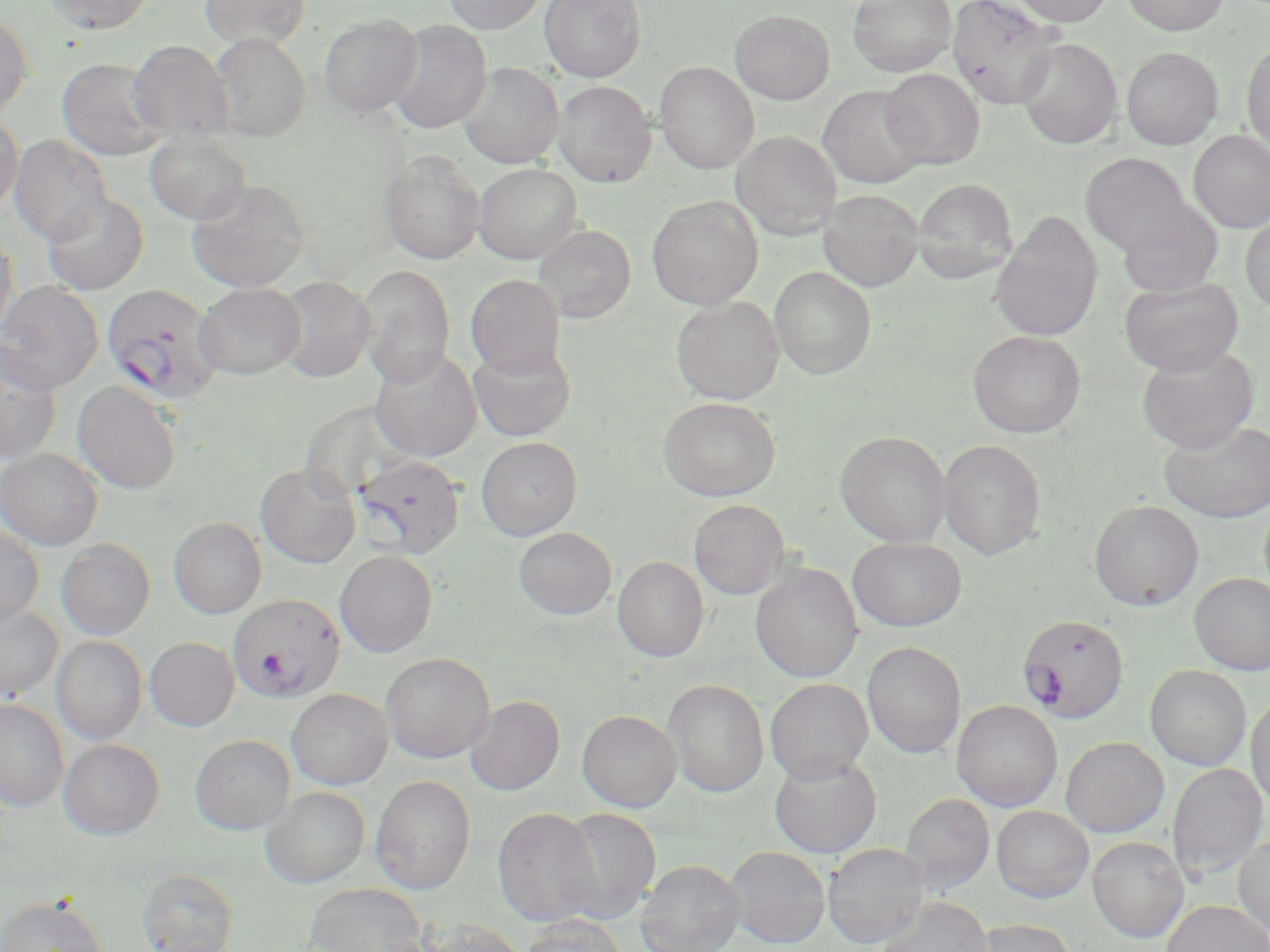
Approximate bounding boxes as (x1,y1)-(x2,y2) corner pairs in pixels. Uninfected red blood cell locations: (44,0)-(156,34), (200,0)-(311,50), (442,0)-(548,34), (540,0)-(647,82), (847,0)-(957,77), (946,0)-(1063,111), (1008,0)-(1115,26), (1121,0)-(1230,36), (729,10)-(835,104), (0,11)-(33,120), (319,13)-(423,117), (387,20)-(492,134), (209,32)-(311,142), (1016,38)-(1123,149), (128,40)-(233,144), (1241,40)-(1270,155), (1121,47)-(1223,150), (56,58)-(168,161), (655,62)-(759,174), (458,63)-(563,168), (880,68)-(984,170), (553,81)-(656,187), (817,85)-(927,189), (0,113)-(23,214), (1189,130)-(1270,232), (145,131)-(252,226), (731,131)-(842,240), (9,134)-(113,245), (381,150)-(485,265), (1080,153)-(1195,258), (474,164)-(582,263), (187,178)-(310,293), (911,178)-(1018,284), (818,189)-(924,292), (42,193)-(149,295), (647,195)-(763,310), (1117,202)-(1223,298), (1240,211)-(1270,316), (989,214)-(1104,342), (533,224)-(635,323), (0,229)-(18,340), (355,264)-(456,387), (769,266)-(876,380), (466,274)-(567,379), (276,276)-(376,383), (1118,277)-(1243,376), (0,280)-(104,393), (194,283)-(306,380), (671,296)-(784,404), (967,330)-(1086,438), (0,342)-(63,465), (468,342)-(576,443), (1137,345)-(1259,453), (369,348)-(482,461), (72,381)-(183,495), (658,397)-(781,500), (1159,419)-(1270,523), (835,431)-(951,547), (476,436)-(582,540), (939,439)-(1046,560), (0,448)-(103,550), (255,464)-(361,568), (689,499)-(790,599), (1088,499)-(1204,610), (168,517)-(267,619), (0,524)-(45,628), (513,527)-(616,619), (847,537)-(967,631), (56,538)-(155,639), (335,550)-(438,657), (613,556)-(709,661), (750,563)-(863,682), (1190,573)-(1270,674), (0,604)-(63,700), (53,635)-(147,745), (145,637)-(240,731), (862,641)-(966,758), (380,651)-(494,763), (1145,665)-(1251,770), (663,678)-(769,798), (765,678)-(873,784), (286,688)-(393,789), (1246,690)-(1270,811), (466,695)-(565,796), (0,698)-(68,812), (952,700)-(1062,811), (577,710)-(682,812), (190,735)-(295,834), (1060,736)-(1169,837), (58,738)-(165,839), (769,753)-(882,858), (1167,763)-(1268,881), (370,775)-(476,895), (261,786)-(370,888), (899,793)-(995,895), (991,805)-(1094,903), (492,807)-(604,927), (558,808)-(661,922), (1234,832)-(1270,940), (1087,836)-(1190,942), (823,843)-(930,949), (724,846)-(831,948), (636,859)-(745,952), (138,869)-(238,951), (303,883)-(429,952), (0,895)-(108,952), (875,897)-(995,952), (1161,899)-(1270,952), (519,915)-(630,952), (419,918)-(531,952), (968,918)-(1077,952). Plasmodium falciparum-infected red blood cell locations: (102,283)-(224,405), (354,454)-(465,560), (228,594)-(345,702), (1017,613)-(1129,724). Slide-level diagnosis: Plasmodium falciparum. One field of a larger specimen. Optical microscopy. Thin blood film. Image is 1270×952 pixels. May-Grünwald-Giemsa-stained preparation. Captured at 1000x magnification.